State which parasite is depicted.
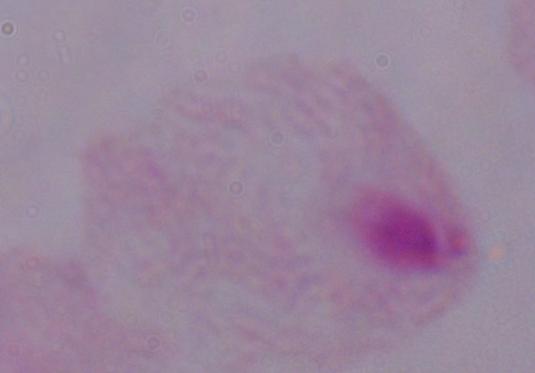
This is a trichomonad.

magnification: 1000x
modality: micrograph